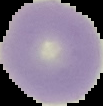

image_type: cell region segmented out of the field of view; surrounding area masked to black
preparation: thin blood film
image_size: 103×106 pixels
malaria_status: uninfected